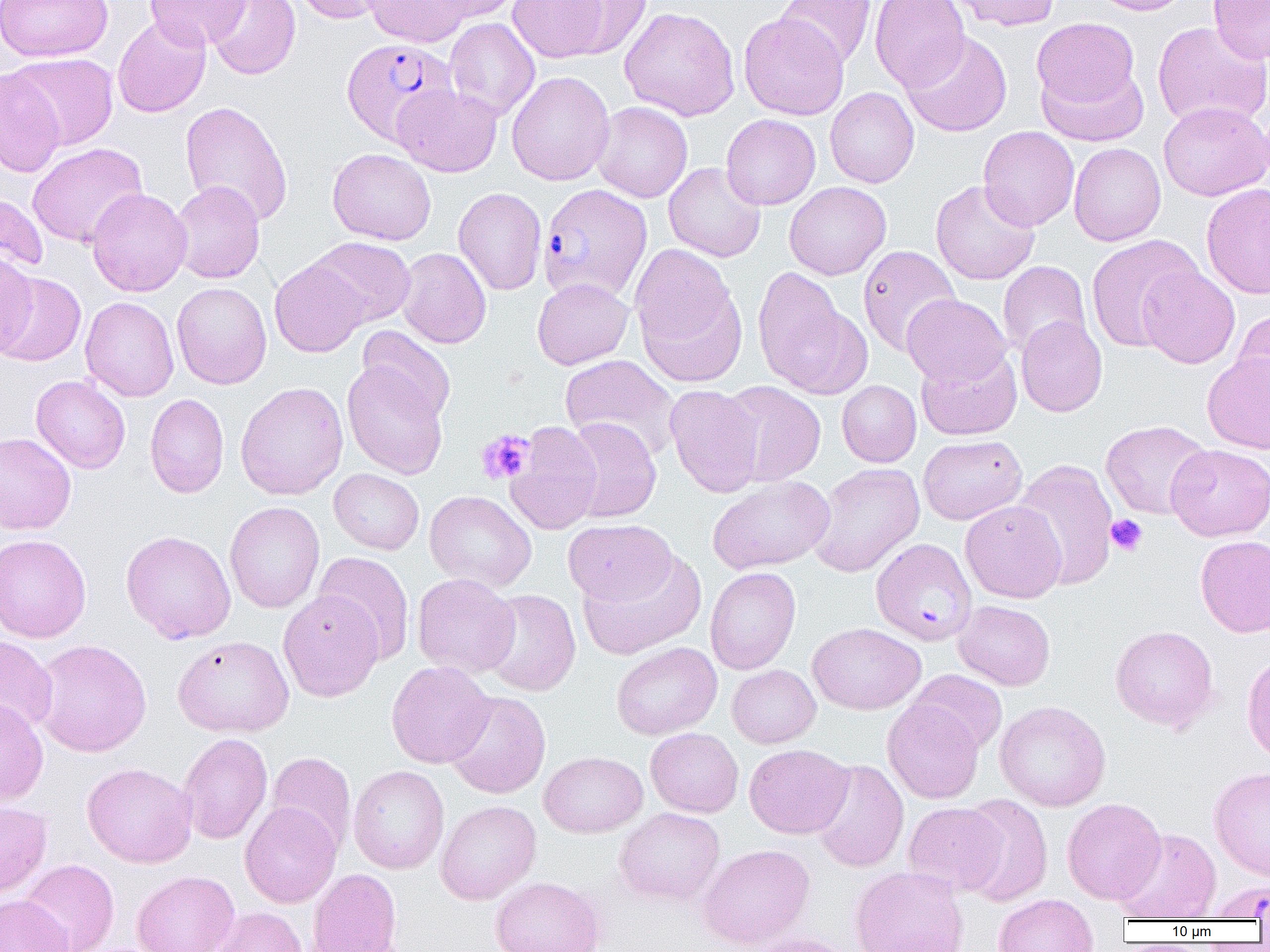 Approximate bounding boxes as (x1,y1)-(x2,y2) corner pairs in pixels. Plasmodium falciparum-infected red blood cell locations: (341,38)-(457,145), (538,183)-(653,304), (871,538)-(977,645), (1204,880)-(1270,920). Uninfected red blood cell locations: (0,0)-(113,62), (145,0)-(250,49), (205,0)-(301,80), (293,0)-(397,25), (364,0)-(472,47), (424,0)-(523,21), (508,0)-(609,62), (558,0)-(652,59), (775,0)-(877,69), (870,0)-(969,91), (947,0)-(1061,31), (1088,0)-(1194,16), (1208,1)-(1270,64), (619,6)-(740,121), (739,12)-(849,120), (112,15)-(211,118), (444,17)-(540,122), (1031,17)-(1141,110), (1152,21)-(1270,130), (900,31)-(1012,137), (6,53)-(119,150), (1036,62)-(1148,146), (0,68)-(66,178), (506,71)-(615,186), (392,83)-(502,177), (825,87)-(919,188), (179,100)-(293,226), (592,101)-(693,203), (1158,101)-(1269,201), (721,114)-(820,210), (978,126)-(1079,231), (27,142)-(148,248), (1068,143)-(1166,246), (327,147)-(437,245), (663,162)-(766,262), (169,180)-(265,283), (930,180)-(1041,285), (784,181)-(891,280), (1201,183)-(1270,299), (86,187)-(192,297), (453,187)-(547,295), (0,192)-(47,277), (1085,234)-(1203,352), (307,236)-(416,328), (629,244)-(743,376), (857,245)-(961,355), (396,247)-(491,349), (0,253)-(38,359), (269,258)-(368,357), (997,261)-(1091,359), (1138,265)-(1240,369), (752,270)-(871,399), (0,272)-(86,367), (532,277)-(633,369), (171,282)-(272,389), (902,294)-(1011,386), (80,296)-(179,401), (1232,307)-(1270,405), (1016,315)-(1107,417), (357,326)-(456,423), (917,348)-(1022,440), (1202,353)-(1270,454), (560,355)-(680,460), (342,362)-(448,479), (31,375)-(130,473), (837,380)-(921,467), (236,381)-(348,500), (721,381)-(825,486), (664,384)-(764,498), (145,393)-(229,498), (562,417)-(662,522), (1100,420)-(1212,519), (506,422)-(602,534), (0,431)-(76,535), (917,434)-(1027,524), (1165,443)-(1270,541), (1013,458)-(1118,590), (808,462)-(925,577), (329,468)-(424,555), (708,475)-(835,574), (424,490)-(537,592), (960,500)-(1067,603), (224,501)-(325,613), (563,519)-(676,605), (121,530)-(236,644), (0,534)-(91,643), (1195,534)-(1270,638), (578,550)-(707,659), (313,551)-(416,664), (705,566)-(801,674), (412,573)-(520,678), (481,589)-(581,697), (278,590)-(384,702), (953,600)-(1056,690), (807,622)-(926,715), (1110,625)-(1219,732), (0,635)-(57,736), (173,635)-(294,737), (32,638)-(152,757), (611,642)-(722,740), (1241,651)-(1270,763), (386,660)-(496,768), (727,664)-(821,748), (907,669)-(1007,755), (444,690)-(551,799), (0,698)-(49,807), (882,699)-(984,803), (994,700)-(1111,811), (646,728)-(743,817), (178,732)-(273,844), (744,743)-(853,838), (539,751)-(648,837), (266,752)-(356,855), (810,759)-(909,872), (82,762)-(197,868), (348,765)-(449,874), (1209,766)-(1270,882), (957,794)-(1054,906), (1062,798)-(1166,904), (435,800)-(542,904), (0,801)-(52,897), (240,801)-(342,908), (903,802)-(1007,895), (614,807)-(725,906), (1112,828)-(1221,921), (696,843)-(815,950), (20,859)-(119,952), (850,865)-(968,952), (307,868)-(402,952), (132,871)-(240,952), (490,876)-(605,952), (0,894)-(73,952), (992,895)-(1099,952), (209,906)-(308,952), (739,932)-(858,952). Platelet locations: (476,429)-(535,485), (1106,514)-(1148,556). Slide-level diagnosis: Plasmodium falciparum. Thin blood film. Light microscopy. Single field of view. 1000x magnification. Image is 1270×952 pixels.